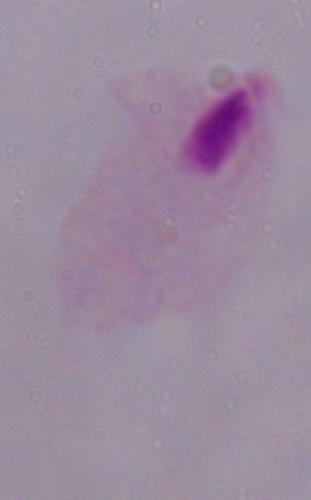 Photomicrograph. A trichomonad is seen. Captured at 1000x magnification.